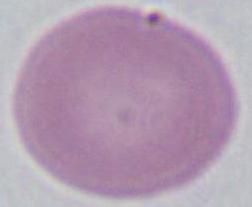
magnification = 1000x
identification = red blood cell
modality = photomicrograph